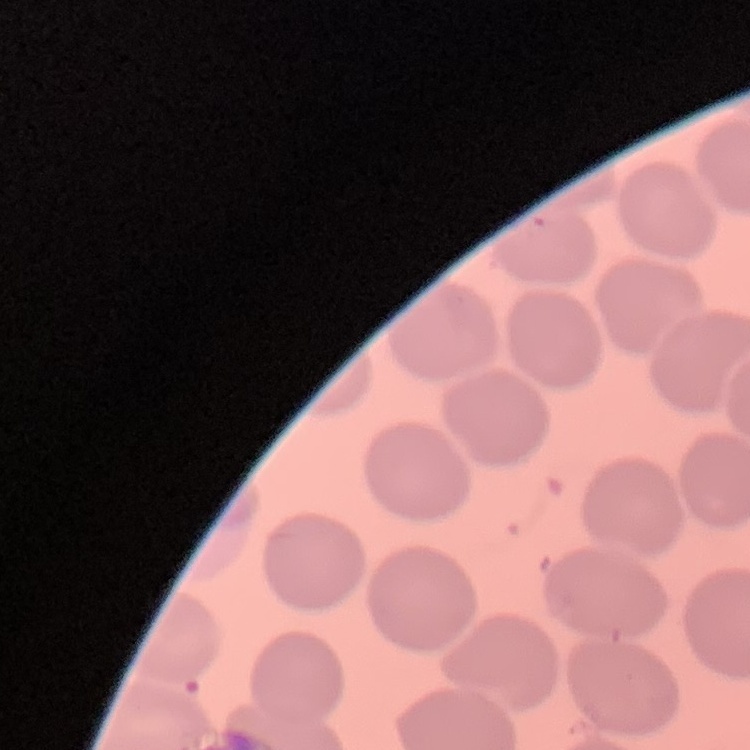
Summary:
  - Red blood cell morphology: no rouleaux formation
  - Image type: square crop of a larger photomicrograph
  - Stain: Field's or Giemsa
  - Preparation: thin blood film